Report the malaria status of this cell.
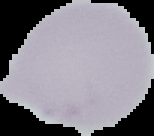
It is uninfected.

preparation = thin blood film
image type = segmented cell region on a black background
image size = 154×136 pixels